Assess this cell for malaria.
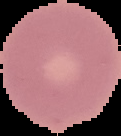
It is uninfected.

{
  "image_type": "cell region segmented out of the field of view; surrounding area masked to black",
  "image_size": "121×136 pixels",
  "preparation": "thin blood film"
}